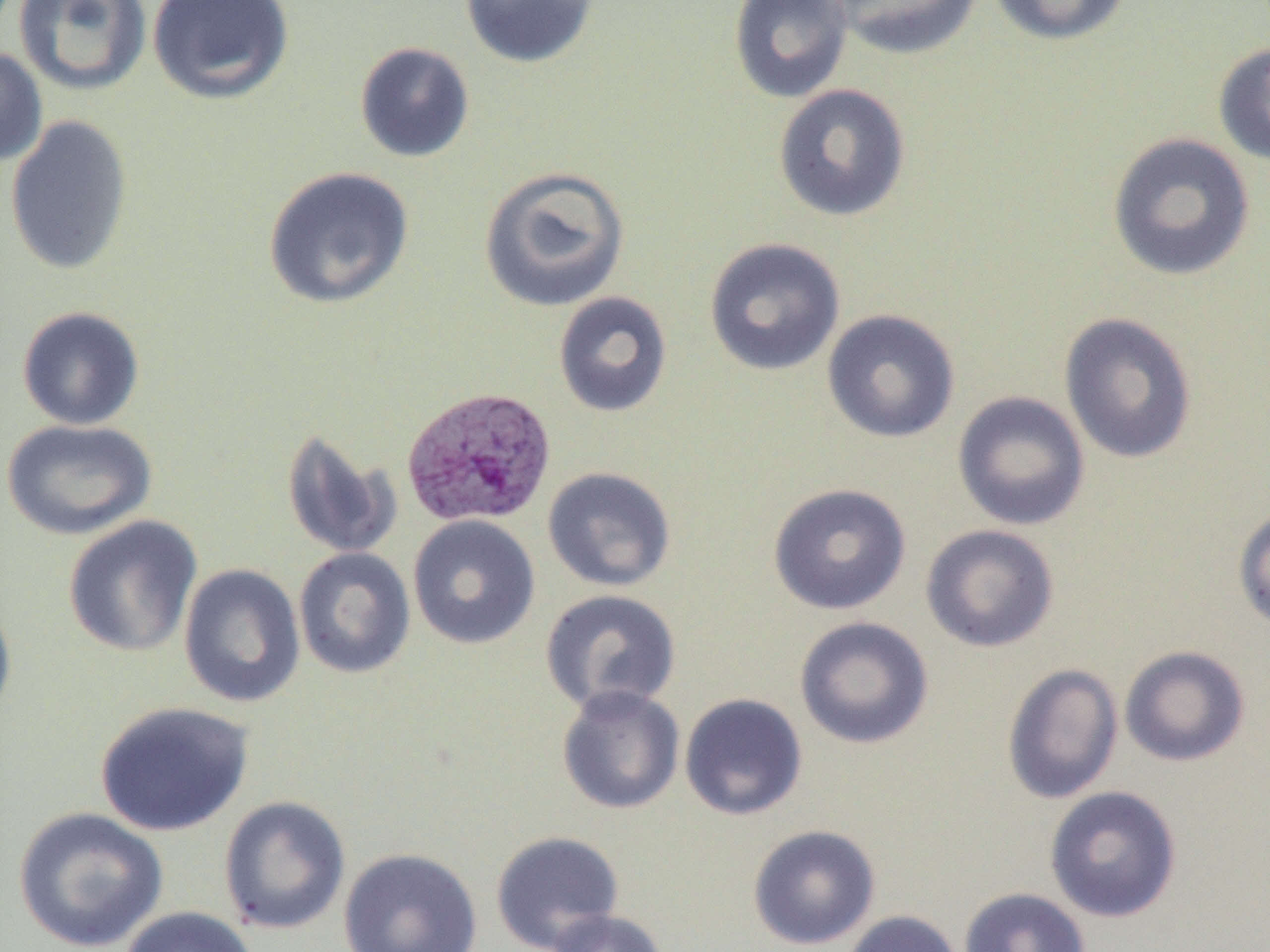 Approximate bounding boxes as (x1, y1, x2, y2) in pixels. Plasmodium vivax-infected red blood cell locations: (401, 386, 556, 528). Uninfected red blood cell locations: (13, 0, 152, 96), (147, 0, 295, 105), (458, 0, 601, 69), (727, 0, 853, 104), (828, 0, 984, 60), (986, 0, 1132, 46), (1213, 40, 1270, 167), (354, 41, 475, 163), (0, 46, 48, 167), (772, 83, 912, 222), (4, 114, 134, 275), (1106, 132, 1256, 282), (478, 165, 631, 313), (262, 166, 415, 310), (703, 237, 846, 377), (553, 291, 673, 418), (16, 305, 145, 430), (822, 308, 961, 444), (1058, 312, 1198, 464), (952, 391, 1091, 531), (1, 418, 157, 540), (281, 429, 402, 560), (542, 466, 676, 592), (767, 482, 911, 615), (1232, 506, 1270, 634), (408, 514, 541, 650), (62, 515, 203, 657), (920, 524, 1060, 653), (293, 547, 416, 679), (179, 563, 306, 709), (539, 589, 682, 715), (0, 590, 17, 732), (793, 616, 935, 750), (1119, 645, 1250, 767), (1001, 663, 1123, 805), (556, 684, 685, 815), (679, 692, 808, 821), (93, 701, 255, 837), (1044, 785, 1183, 923), (218, 795, 351, 935), (13, 806, 169, 952), (747, 824, 881, 950), (490, 830, 624, 952), (338, 847, 483, 952), (958, 887, 1091, 952), (119, 906, 259, 952), (545, 908, 669, 952), (841, 909, 964, 952). Slide-level diagnosis: Plasmodium vivax. Thin blood film. Light microscopy. Single field of view. Captured at 1000x magnification. Image is 1270×952 pixels.